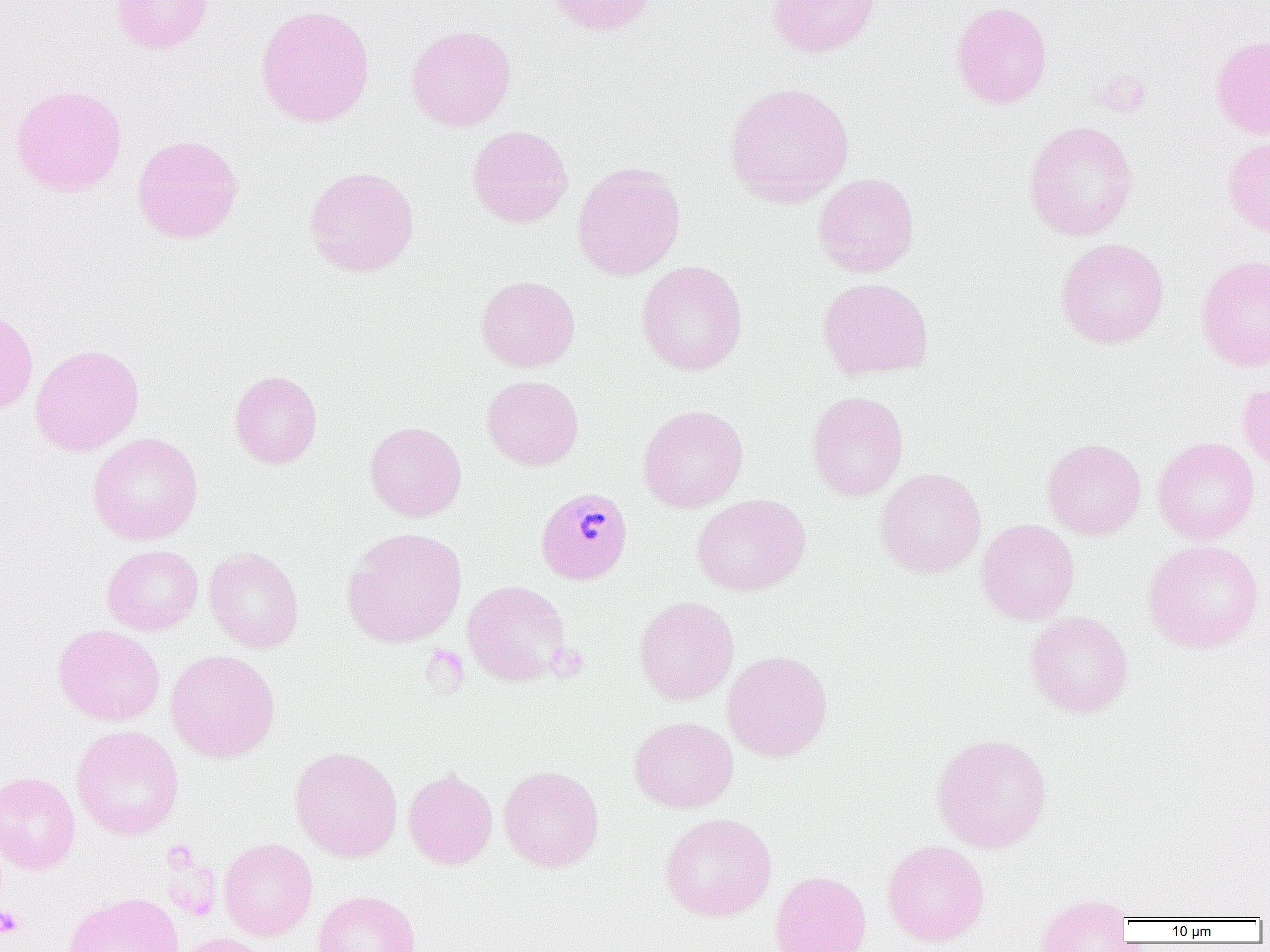

Approximate bounding boxes as (x1,y1)-(x2,y2) corner pairs in pixels. Platelet locations: (1092,70)-(1151,118), (548,643)-(589,681), (0,905)-(24,939). Uninfected red blood cell locations: (111,0)-(214,55), (544,0)-(657,36), (767,0)-(881,58), (951,1)-(1053,109), (255,4)-(376,128), (406,24)-(516,132), (1210,34)-(1270,140), (723,82)-(854,208), (10,84)-(127,198), (1023,120)-(1138,241), (467,125)-(573,228), (132,134)-(244,245), (1223,137)-(1270,239), (572,162)-(686,281), (304,166)-(419,277), (813,173)-(919,277), (1056,237)-(1169,349), (1196,255)-(1270,372), (636,260)-(748,376), (476,275)-(580,373), (817,277)-(934,381), (0,305)-(39,414), (30,343)-(145,457), (229,370)-(322,469), (482,375)-(584,471), (1237,382)-(1270,476), (806,390)-(909,501), (638,404)-(748,514), (364,421)-(467,522), (87,432)-(204,545), (1153,436)-(1260,545), (1042,438)-(1146,540), (875,467)-(986,579), (692,493)-(811,596), (976,519)-(1079,625), (342,527)-(467,648), (1142,539)-(1264,654), (102,544)-(203,636), (204,547)-(304,654), (463,580)-(571,687), (633,595)-(739,705), (1025,612)-(1133,718), (53,624)-(165,727), (166,649)-(280,763), (723,649)-(833,762), (628,716)-(738,813), (71,725)-(184,841), (931,732)-(1052,853), (290,746)-(402,863), (499,765)-(604,872), (403,768)-(498,869), (0,770)-(80,875), (659,812)-(777,922), (218,838)-(317,941), (882,840)-(990,947), (769,870)-(872,952), (311,890)-(421,952), (64,891)-(183,952), (1035,893)-(1133,952), (173,933)-(270,952). Plasmodium malariae-infected red blood cell locations: (536,487)-(632,584). Slide-level diagnosis: Plasmodium malariae. Thin blood film. Light microscopy. Single field of view. Captured at 1000x magnification. Image is 1270×952 pixels.